Point out cells.
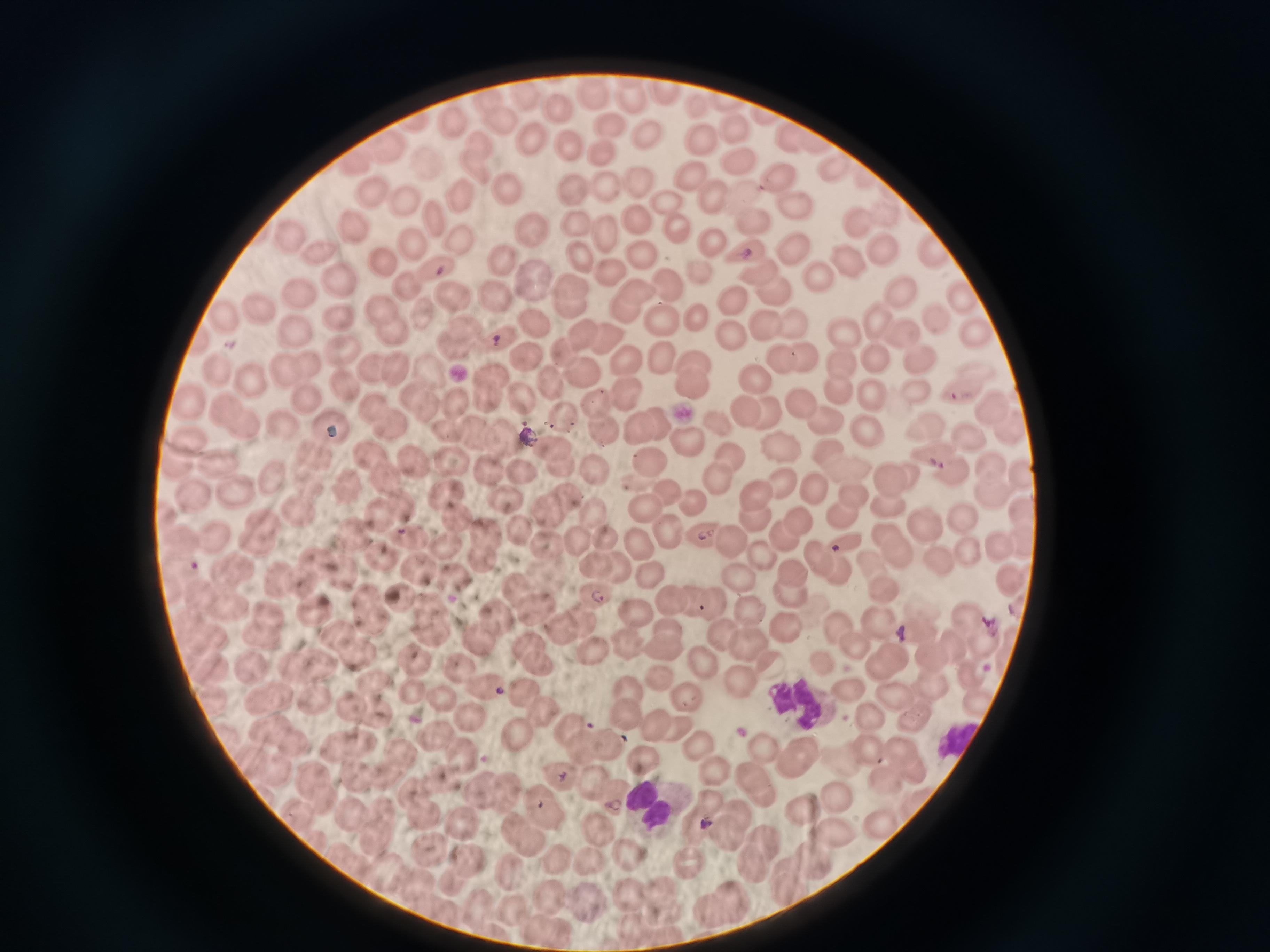
Approximate object centers, in pixels from the top-left corner.
Cells: (x=662, y=89), (x=596, y=95), (x=635, y=98), (x=495, y=104), (x=557, y=111), (x=413, y=123), (x=457, y=123), (x=503, y=124), (x=608, y=126), (x=738, y=129), (x=646, y=131), (x=529, y=138), (x=789, y=139), (x=700, y=140), (x=479, y=143), (x=820, y=143), (x=567, y=145), (x=388, y=150), (x=600, y=153), (x=357, y=161), (x=430, y=163), (x=742, y=163), (x=834, y=163), (x=479, y=169), (x=693, y=176), (x=785, y=179), (x=639, y=183), (x=507, y=188), (x=576, y=189), (x=603, y=190), (x=376, y=191), (x=462, y=195), (x=712, y=197), (x=747, y=199), (x=403, y=200), (x=668, y=204), (x=797, y=206), (x=438, y=216), (x=856, y=218), (x=751, y=222), (x=355, y=226), (x=575, y=226), (x=639, y=227), (x=533, y=229), (x=607, y=231), (x=681, y=234), (x=291, y=235), (x=710, y=243), (x=415, y=244), (x=463, y=246), (x=880, y=248), (x=790, y=251), (x=323, y=253), (x=750, y=253), (x=644, y=255), (x=936, y=255), (x=500, y=256), (x=847, y=257), (x=581, y=258), (x=388, y=263), (x=441, y=268), (x=611, y=268), (x=704, y=271), (x=756, y=274), (x=338, y=275), (x=532, y=275), (x=814, y=276), (x=408, y=283), (x=573, y=283), (x=668, y=284), (x=637, y=286), (x=901, y=288), (x=305, y=293), (x=962, y=294), (x=496, y=295), (x=772, y=296), (x=451, y=299), (x=569, y=304), (x=735, y=305), (x=386, y=307), (x=625, y=309), (x=263, y=310), (x=424, y=310), (x=696, y=315), (x=339, y=316), (x=938, y=316), (x=877, y=317), (x=221, y=319), (x=661, y=319), (x=791, y=321), (x=765, y=326), (x=390, y=327), (x=536, y=327), (x=898, y=329), (x=467, y=330), (x=293, y=331), (x=581, y=333), (x=974, y=333), (x=500, y=334), (x=847, y=334), (x=608, y=336), (x=730, y=338), (x=344, y=345), (x=452, y=347), (x=563, y=350), (x=808, y=353), (x=661, y=356), (x=919, y=356), (x=786, y=357), (x=880, y=357), (x=526, y=358), (x=839, y=359), (x=625, y=361), (x=692, y=361), (x=312, y=365), (x=221, y=367), (x=398, y=367), (x=374, y=368), (x=281, y=372), (x=428, y=372), (x=580, y=372), (x=492, y=373), (x=252, y=378), (x=755, y=379), (x=547, y=382), (x=346, y=385), (x=692, y=385), (x=917, y=386), (x=837, y=389), (x=871, y=389), (x=518, y=390), (x=624, y=390), (x=410, y=393), (x=304, y=394), (x=965, y=395), (x=486, y=397), (x=453, y=398), (x=189, y=401), (x=597, y=401), (x=801, y=403), (x=425, y=404), (x=741, y=407), (x=991, y=407), (x=376, y=408), (x=230, y=409), (x=762, y=410), (x=560, y=416), (x=823, y=417), (x=242, y=421), (x=286, y=421), (x=659, y=422), (x=924, y=423), (x=388, y=424), (x=714, y=424), (x=333, y=425), (x=861, y=425), (x=1010, y=425), (x=602, y=426), (x=639, y=428), (x=447, y=429), (x=963, y=432), (x=472, y=433), (x=505, y=437), (x=191, y=438), (x=685, y=440), (x=559, y=450), (x=780, y=450), (x=934, y=452), (x=315, y=453), (x=725, y=453), (x=832, y=453), (x=448, y=455), (x=647, y=456), (x=371, y=457), (x=216, y=458), (x=418, y=460), (x=559, y=465), (x=987, y=466), (x=178, y=467), (x=522, y=467), (x=846, y=467), (x=489, y=469), (x=597, y=472), (x=278, y=473), (x=912, y=473), (x=948, y=473), (x=888, y=475), (x=390, y=476), (x=1017, y=477), (x=715, y=479), (x=785, y=479), (x=817, y=481), (x=310, y=483), (x=350, y=484), (x=667, y=487), (x=445, y=491), (x=986, y=491), (x=238, y=493), (x=761, y=494), (x=196, y=495), (x=854, y=495), (x=508, y=497), (x=567, y=498), (x=694, y=498), (x=399, y=502), (x=643, y=504), (x=888, y=508), (x=547, y=510), (x=298, y=512), (x=377, y=512), (x=1018, y=512), (x=454, y=514), (x=593, y=514), (x=842, y=515), (x=958, y=515), (x=265, y=519), (x=754, y=519), (x=796, y=521), (x=665, y=523), (x=924, y=525), (x=517, y=528), (x=484, y=529), (x=884, y=532), (x=354, y=534), (x=779, y=536), (x=216, y=537), (x=603, y=537), (x=705, y=537), (x=576, y=538), (x=415, y=539), (x=727, y=539), (x=841, y=540), (x=255, y=543), (x=545, y=543), (x=445, y=544), (x=641, y=544), (x=1020, y=544), (x=997, y=545), (x=483, y=553), (x=905, y=553), (x=973, y=553), (x=758, y=555), (x=819, y=556), (x=383, y=558), (x=316, y=560), (x=873, y=560), (x=594, y=561), (x=941, y=561), (x=617, y=564), (x=233, y=568), (x=416, y=570), (x=839, y=570), (x=792, y=572), (x=342, y=573), (x=647, y=574), (x=734, y=574), (x=298, y=580), (x=278, y=582), (x=457, y=582), (x=1009, y=583), (x=220, y=585), (x=884, y=587), (x=516, y=588), (x=791, y=589), (x=203, y=592), (x=593, y=592), (x=400, y=593), (x=362, y=597), (x=694, y=598), (x=713, y=599), (x=670, y=601), (x=228, y=606), (x=428, y=606), (x=747, y=607), (x=534, y=611), (x=266, y=612), (x=314, y=612), (x=638, y=612), (x=369, y=617), (x=494, y=619), (x=582, y=622), (x=880, y=622), (x=970, y=622), (x=666, y=624), (x=839, y=627), (x=719, y=629), (x=790, y=630), (x=560, y=631), (x=437, y=633), (x=262, y=634), (x=337, y=634), (x=921, y=637), (x=476, y=639), (x=745, y=639), (x=528, y=641), (x=981, y=642), (x=628, y=643), (x=857, y=644), (x=953, y=647), (x=666, y=648), (x=597, y=650), (x=357, y=651), (x=895, y=653), (x=932, y=657), (x=320, y=660), (x=419, y=661), (x=708, y=662), (x=539, y=663), (x=294, y=665), (x=822, y=665), (x=250, y=667), (x=876, y=667), (x=462, y=668), (x=773, y=669), (x=968, y=672), (x=664, y=679), (x=371, y=680), (x=743, y=680), (x=489, y=687), (x=934, y=687), (x=521, y=688), (x=628, y=689), (x=412, y=691), (x=844, y=695), (x=894, y=696), (x=261, y=697), (x=312, y=697), (x=438, y=697), (x=688, y=699), (x=974, y=699), (x=284, y=700), (x=347, y=700), (x=214, y=704), (x=542, y=709), (x=821, y=709), (x=623, y=714), (x=374, y=716), (x=871, y=717), (x=471, y=718), (x=921, y=718), (x=652, y=719), (x=567, y=725), (x=267, y=726), (x=515, y=732), (x=679, y=732), (x=437, y=733), (x=292, y=742), (x=367, y=742), (x=613, y=745), (x=340, y=747), (x=582, y=747), (x=704, y=747), (x=763, y=747), (x=867, y=747), (x=900, y=748), (x=806, y=749), (x=410, y=754), (x=461, y=754), (x=645, y=761), (x=798, y=762), (x=254, y=763), (x=274, y=768), (x=913, y=769), (x=714, y=773), (x=753, y=774), (x=352, y=775), (x=312, y=778), (x=563, y=778), (x=886, y=778), (x=382, y=781), (x=441, y=784), (x=596, y=785), (x=414, y=790), (x=484, y=790), (x=509, y=790), (x=758, y=795), (x=836, y=795), (x=614, y=796), (x=537, y=800), (x=321, y=803), (x=735, y=810), (x=807, y=811), (x=384, y=812), (x=300, y=815), (x=353, y=815), (x=424, y=817), (x=878, y=818), (x=550, y=819), (x=696, y=820), (x=468, y=822), (x=602, y=828), (x=833, y=828), (x=729, y=831), (x=514, y=833), (x=759, y=833), (x=373, y=841), (x=429, y=852), (x=630, y=855), (x=689, y=855), (x=554, y=856), (x=813, y=856), (x=474, y=861), (x=586, y=861), (x=751, y=863), (x=511, y=871), (x=454, y=880), (x=789, y=880), (x=661, y=889), (x=732, y=895), (x=588, y=896), (x=635, y=896), (x=553, y=898), (x=712, y=906), (x=663, y=909), (x=515, y=911), (x=637, y=926).

malaria_reading: positive
stain: Giemsa
capture: smartphone through the microscope eyepiece
image_size: 1270×952 pixels
field_of_view: single
preparation: thin blood film